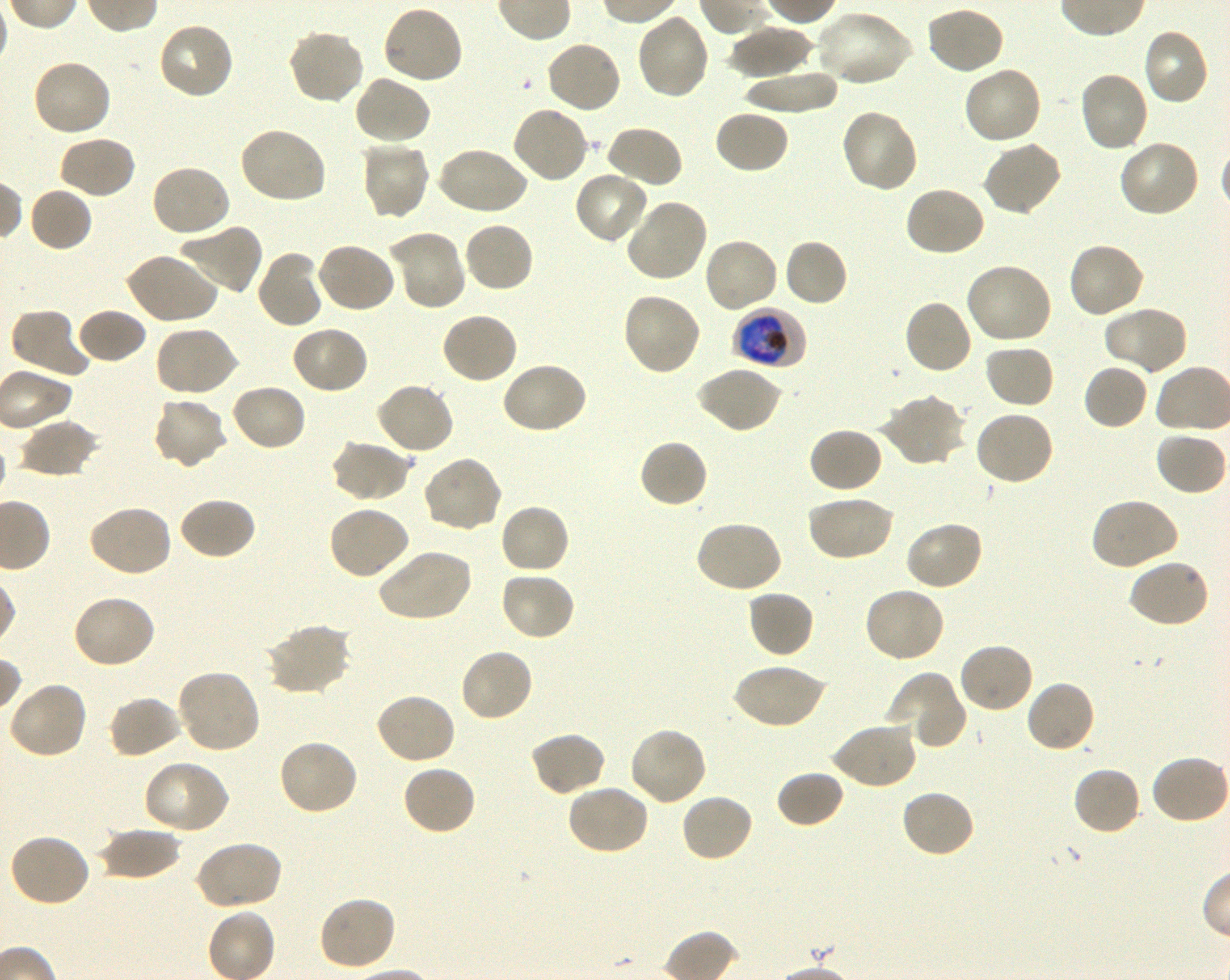
Not every red blood cell is marked. A life-cycle stage — or a range of stages, where the recorded stages span more than one — follows each staged infected red blood cell.
preparation: thin blood film
locations_of_uninfected_red_blood_cells: 'approximate bounding boxes as {x1, y1, x2, y2} in pixels: {382, 3, 465, 85}, {924, 5, 1006, 76}, {814, 10, 914, 87}, {635, 13, 711, 101}, {156, 21, 236, 101}, {728, 25, 813, 78}, {1141, 26, 1210, 106}, {286, 28, 366, 105}, {545, 39, 623, 115}, {31, 58, 114, 138}, {962, 65, 1044, 146}, {742, 69, 841, 114}, {1077, 71, 1150, 154}, {353, 75, 433, 146}, {511, 104, 591, 183}, {713, 109, 790, 176}, {838, 109, 919, 194}, {602, 125, 684, 190}, {237, 126, 327, 205}, {58, 135, 137, 199}, {359, 139, 431, 221}, {982, 140, 1063, 217}, {1117, 140, 1202, 219}, {436, 145, 529, 216}, {150, 163, 232, 238}, {573, 170, 650, 246}, {903, 185, 987, 258}, {29, 187, 93, 253}, {623, 198, 709, 283}, {462, 220, 534, 295}, {177, 223, 264, 296}, {388, 229, 466, 310}, {702, 237, 779, 314}, {783, 238, 849, 308}, {1067, 240, 1146, 319}, {316, 242, 397, 314}, {256, 250, 326, 330}, {124, 251, 220, 325}, {963, 262, 1053, 346}, {620, 292, 702, 377}, {902, 299, 974, 376}, {1102, 305, 1188, 376}, {9, 307, 91, 379}, {75, 308, 147, 365}, {439, 311, 518, 385}, {289, 324, 370, 395}, {152, 325, 240, 398}, {983, 345, 1056, 410}, {500, 360, 589, 435}, {1082, 362, 1149, 431}, {695, 365, 782, 434}, {375, 381, 456, 456}, {230, 382, 308, 452}, {878, 394, 967, 468}, {151, 396, 229, 470}, {974, 409, 1056, 487}, {18, 418, 101, 478}, {807, 427, 885, 494}, {1154, 431, 1227, 496}, {638, 438, 709, 509}, {329, 439, 413, 503}, {421, 455, 504, 534}, {805, 494, 896, 562}, {178, 496, 257, 561}, {1089, 497, 1180, 571}, {499, 503, 570, 575}, {87, 504, 173, 579}, {326, 504, 412, 581}, {695, 519, 784, 594}, {904, 519, 985, 591}, {377, 547, 473, 622}, {1128, 557, 1211, 629}, {498, 570, 577, 642}, {862, 585, 947, 663}, {746, 589, 814, 659}, {70, 593, 157, 670}, {264, 622, 352, 696}, {956, 641, 1034, 714}, {459, 647, 534, 724}, {733, 662, 827, 730}, {175, 668, 263, 754}, {887, 671, 966, 748}, {7, 680, 89, 760}, {1024, 680, 1097, 754}, {373, 692, 457, 766}, {107, 695, 183, 760}, {830, 721, 917, 790}, {628, 726, 709, 808}, {528, 731, 607, 797}, {277, 739, 359, 816}, {1151, 753, 1230, 825}, {141, 760, 230, 836}, {401, 763, 477, 836}, {1071, 765, 1143, 836}, {775, 769, 846, 829}, {565, 782, 650, 856}, {899, 788, 976, 859}, {680, 792, 754, 863}, {98, 824, 181, 881}, {8, 832, 91, 908}, {192, 840, 282, 911}, {317, 895, 398, 972}'
field_of_view: single
image_size: 1230×980 pixels
stain: Giemsa
culture: shaking in-vitro P. falciparum strain 3D7
donor_blood_group: O+
objective: 100x, oil immersion, numerical aperture 1.30
locations_of_infected_red_blood_cells: 'approximate bounding boxes as {x1, y1, x2, y2} in pixels: {733, 307, 807, 369} early trophozoite to early schizont'